Name the blood parasite species.
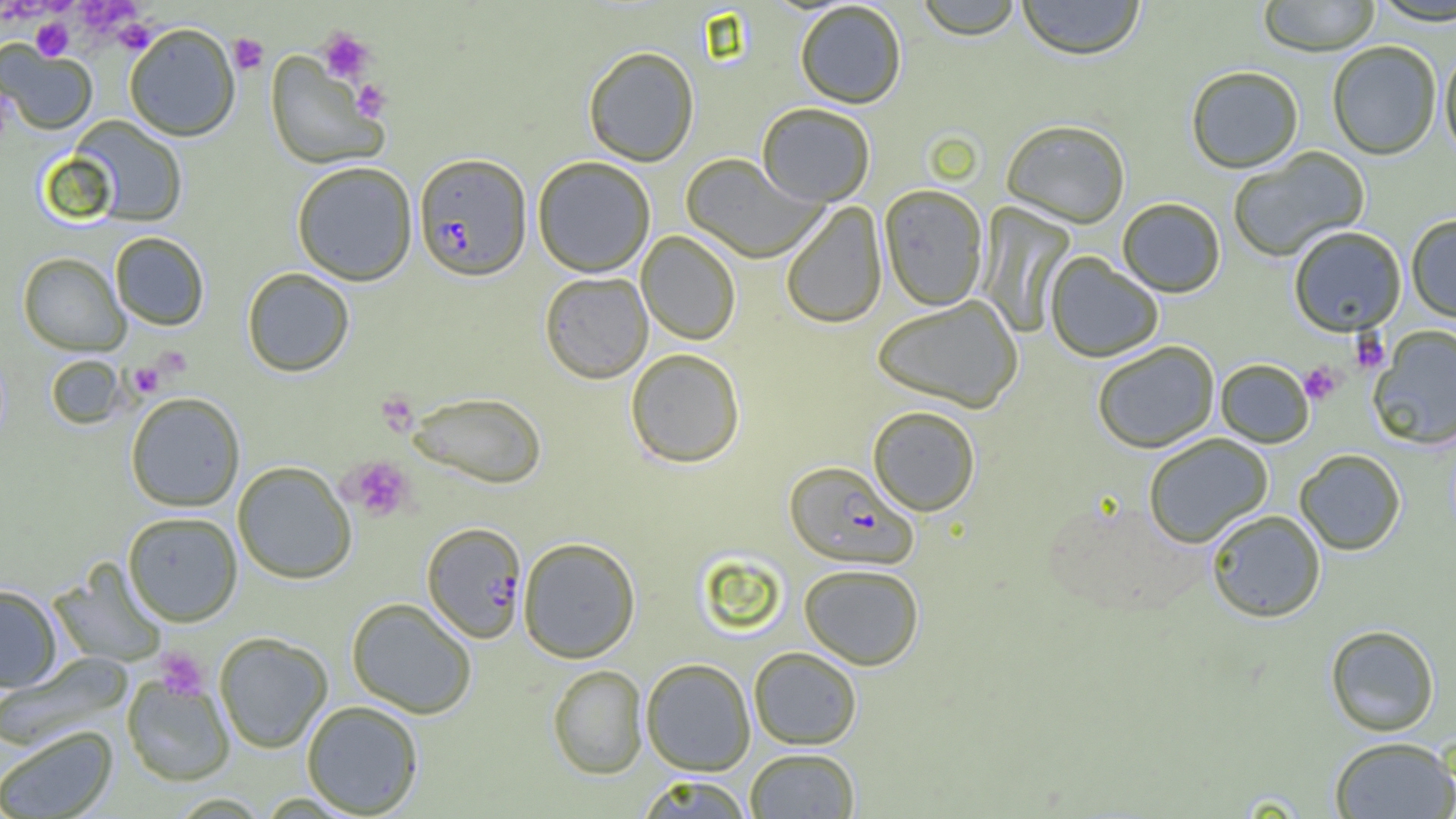
Plasmodium falciparum.

uninfected red blood cell locations = approximate bounding boxes as named x1/y1/x2/y2 corners in pixels: (x1=915, y1=0, x2=1023, y2=39), (x1=1016, y1=0, x2=1146, y2=60), (x1=1257, y1=0, x2=1381, y2=56), (x1=1369, y1=0, x2=1456, y2=25), (x1=794, y1=1, x2=907, y2=109), (x1=124, y1=22, x2=241, y2=141), (x1=0, y1=41, x2=97, y2=135), (x1=1327, y1=41, x2=1442, y2=159), (x1=583, y1=46, x2=699, y2=166), (x1=1439, y1=46, x2=1456, y2=161), (x1=265, y1=52, x2=389, y2=170), (x1=1186, y1=65, x2=1304, y2=173), (x1=757, y1=102, x2=876, y2=206), (x1=70, y1=116, x2=187, y2=227), (x1=1001, y1=118, x2=1131, y2=228), (x1=1227, y1=146, x2=1370, y2=262), (x1=681, y1=153, x2=827, y2=263), (x1=533, y1=156, x2=656, y2=277), (x1=291, y1=160, x2=418, y2=286), (x1=878, y1=184, x2=988, y2=311), (x1=1116, y1=197, x2=1226, y2=297), (x1=780, y1=202, x2=887, y2=329), (x1=977, y1=202, x2=1076, y2=338), (x1=1406, y1=214, x2=1456, y2=323), (x1=1288, y1=225, x2=1407, y2=336), (x1=636, y1=230, x2=741, y2=345), (x1=110, y1=232, x2=209, y2=330), (x1=18, y1=252, x2=129, y2=355), (x1=1045, y1=252, x2=1163, y2=363), (x1=242, y1=268, x2=354, y2=377), (x1=539, y1=271, x2=653, y2=383), (x1=872, y1=295, x2=1025, y2=412), (x1=1368, y1=325, x2=1456, y2=450), (x1=1092, y1=340, x2=1220, y2=453), (x1=625, y1=348, x2=745, y2=468), (x1=45, y1=354, x2=128, y2=430), (x1=1215, y1=358, x2=1314, y2=448), (x1=408, y1=391, x2=547, y2=488), (x1=125, y1=392, x2=246, y2=512), (x1=867, y1=405, x2=981, y2=516), (x1=1143, y1=432, x2=1273, y2=548), (x1=1294, y1=449, x2=1406, y2=555), (x1=232, y1=461, x2=357, y2=584), (x1=1205, y1=509, x2=1326, y2=623), (x1=123, y1=511, x2=243, y2=626), (x1=518, y1=537, x2=641, y2=663), (x1=49, y1=559, x2=169, y2=668), (x1=798, y1=563, x2=925, y2=669), (x1=0, y1=584, x2=62, y2=692), (x1=346, y1=598, x2=478, y2=718), (x1=1324, y1=624, x2=1441, y2=736), (x1=214, y1=632, x2=333, y2=753), (x1=748, y1=646, x2=862, y2=749), (x1=1, y1=652, x2=133, y2=751), (x1=641, y1=658, x2=755, y2=775), (x1=548, y1=664, x2=648, y2=779), (x1=122, y1=675, x2=235, y2=786), (x1=301, y1=700, x2=424, y2=817), (x1=0, y1=725, x2=119, y2=819), (x1=1328, y1=735, x2=1456, y2=818), (x1=745, y1=747, x2=860, y2=818), (x1=636, y1=775, x2=753, y2=819)
field of view = single
magnification = 1000x
modality = light microscopy
platelet locations = approximate bounding boxes as named x1/y1/x2/y2 corners in pixels: (x1=73, y1=1, x2=143, y2=37), (x1=31, y1=17, x2=73, y2=60), (x1=112, y1=18, x2=158, y2=55), (x1=317, y1=28, x2=374, y2=82), (x1=228, y1=33, x2=269, y2=75), (x1=351, y1=79, x2=392, y2=120), (x1=1349, y1=331, x2=1390, y2=374), (x1=153, y1=346, x2=192, y2=379), (x1=135, y1=353, x2=182, y2=387), (x1=1299, y1=361, x2=1343, y2=405), (x1=128, y1=362, x2=164, y2=398), (x1=376, y1=390, x2=419, y2=436), (x1=342, y1=455, x2=415, y2=521), (x1=154, y1=648, x2=210, y2=700)
preparation = thin blood smear
Plasmodium falciparum-infected red blood cell locations = approximate bounding boxes as named x1/y1/x2/y2 corners in pixels: (x1=414, y1=152, x2=532, y2=281), (x1=783, y1=460, x2=918, y2=569), (x1=422, y1=522, x2=528, y2=644)
image size = 1456×819 pixels